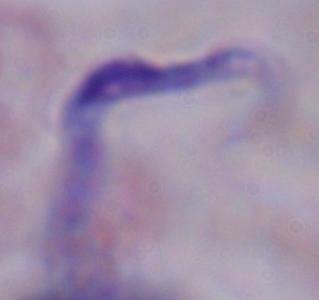 A trypanosome is shown. 1000x magnification. Photomicrograph.